Assess for malaria.
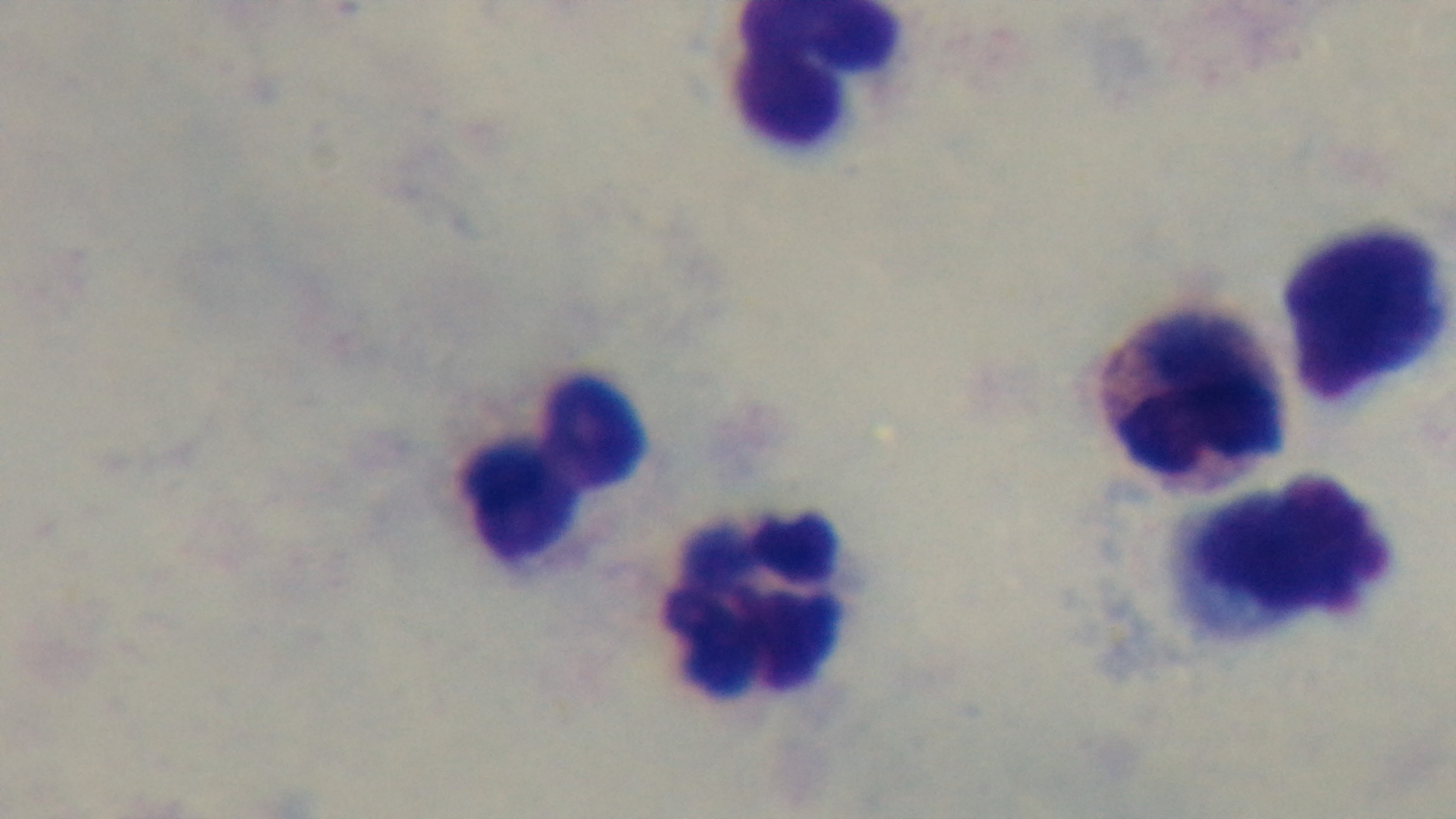
Negative.

Light microscopy. Captured with a mounted 4K digital camera. 100x oil-immersion objective. Single field of view. Preparation: thick blood film. Giemsa-stained.